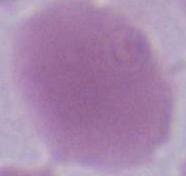
Summary:
  - Magnification: 1000x
  - Identification: erythrocyte
  - Modality: photomicrograph